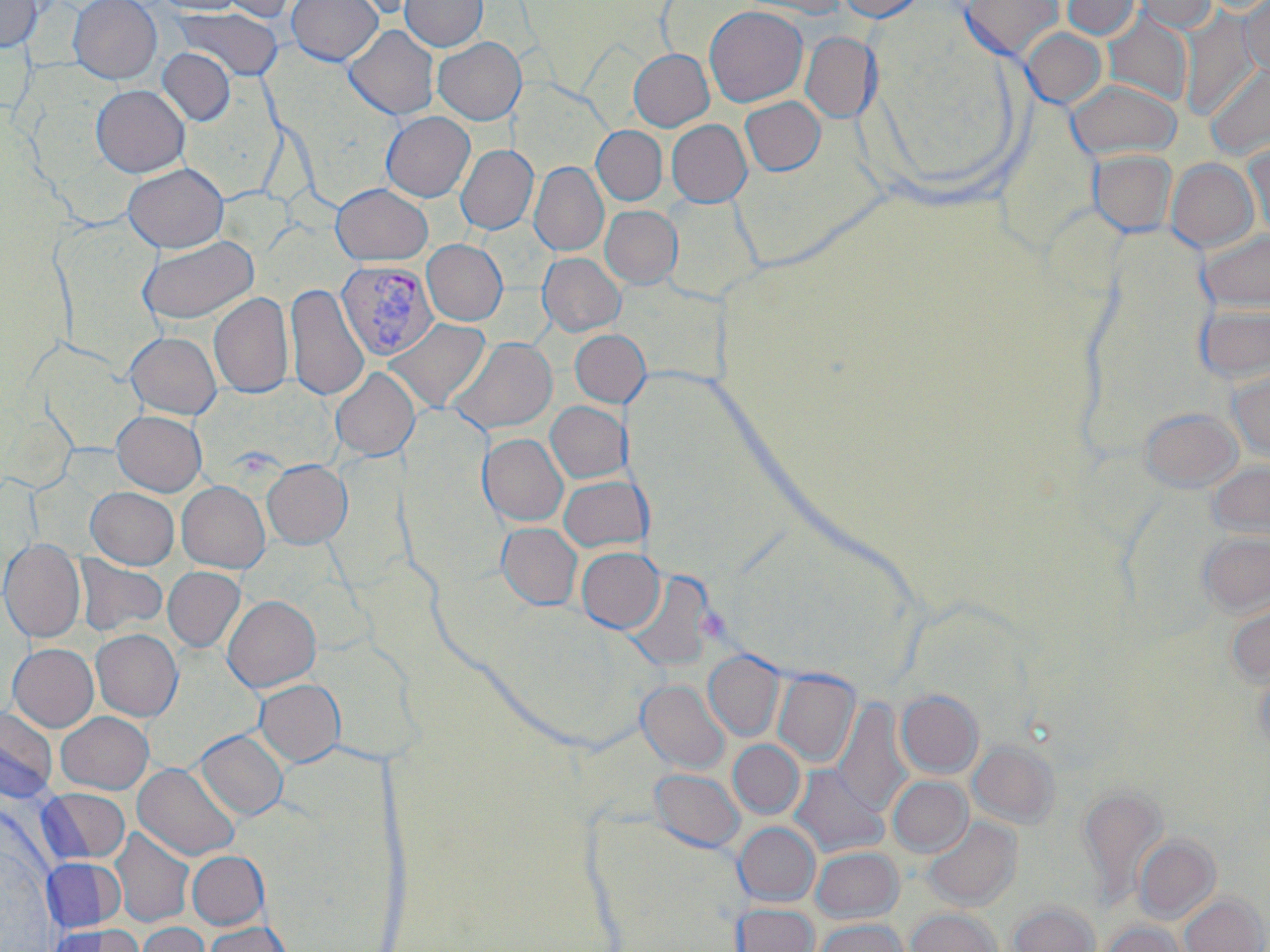
Plasmodium vivax-infected red blood cell locations = approximate bounding boxes as (x1, y1, x2, y2) in pixels: (336, 259, 438, 361)
slide-level diagnosis = Plasmodium vivax
magnification = 1000x
preparation = thin blood smear
field of view = single
image size = 1270×952 pixels
stain = May-Grünwald-Giemsa
uninfected red blood cell locations = approximate bounding boxes as (x1, y1, x2, y2) in pixels: (0, 0, 43, 52), (68, 0, 162, 84), (152, 0, 249, 15), (218, 0, 301, 23), (286, 0, 383, 65), (332, 0, 423, 19), (400, 0, 487, 52), (734, 0, 850, 18), (836, 0, 927, 22), (960, 0, 1063, 62), (1061, 0, 1141, 40), (1131, 0, 1218, 33), (1239, 0, 1270, 79), (704, 5, 808, 107), (174, 7, 283, 81), (1103, 13, 1192, 106), (1179, 13, 1260, 119), (344, 25, 439, 120), (1021, 27, 1106, 110), (801, 32, 880, 123), (433, 37, 526, 125), (158, 48, 235, 126), (629, 49, 714, 131), (1205, 63, 1269, 161), (1066, 78, 1182, 161), (91, 85, 190, 177), (740, 96, 825, 175), (381, 111, 475, 201), (666, 120, 751, 207), (591, 126, 667, 205), (1244, 139, 1270, 239), (456, 145, 538, 234), (1089, 150, 1177, 237), (1166, 158, 1258, 253), (529, 162, 608, 256), (123, 163, 228, 253), (331, 183, 433, 265), (659, 193, 764, 304), (600, 205, 682, 289), (1197, 230, 1270, 313), (138, 236, 259, 325), (422, 240, 507, 325), (538, 252, 625, 336), (285, 283, 369, 402), (208, 292, 294, 398), (1195, 303, 1270, 385), (385, 318, 491, 412), (570, 329, 650, 407), (125, 331, 222, 419), (449, 337, 557, 434), (1228, 365, 1270, 462), (330, 367, 419, 460), (546, 401, 630, 483), (1139, 407, 1242, 493), (111, 410, 207, 496), (478, 433, 567, 526), (262, 459, 352, 548), (1207, 461, 1270, 545), (558, 475, 649, 553), (177, 481, 269, 572), (86, 487, 178, 569), (497, 522, 582, 611), (1198, 530, 1270, 619), (0, 538, 85, 642), (576, 547, 664, 633), (76, 555, 168, 638), (163, 567, 245, 652), (622, 572, 716, 673), (223, 595, 321, 692), (1224, 596, 1270, 688), (91, 629, 183, 721), (8, 643, 99, 732), (704, 651, 784, 740), (1253, 664, 1270, 759), (773, 671, 859, 766), (254, 679, 345, 767), (637, 679, 729, 773), (896, 690, 983, 778), (831, 700, 912, 819), (0, 708, 58, 802), (56, 711, 153, 794), (195, 729, 289, 821), (728, 740, 804, 819), (968, 740, 1060, 828), (132, 762, 240, 860), (791, 765, 888, 858), (649, 769, 744, 853), (888, 776, 972, 857), (1078, 785, 1166, 906), (38, 788, 130, 864), (577, 809, 753, 952), (923, 816, 1021, 911), (734, 822, 820, 906), (109, 828, 194, 928), (1134, 835, 1220, 923), (810, 847, 903, 923), (187, 851, 269, 930), (42, 858, 116, 933), (1180, 893, 1267, 952), (1009, 901, 1099, 952), (733, 903, 818, 952), (907, 908, 1002, 952), (813, 919, 907, 952), (204, 921, 289, 952), (1100, 921, 1188, 952), (135, 922, 210, 952), (49, 924, 141, 952)
modality = light microscopy